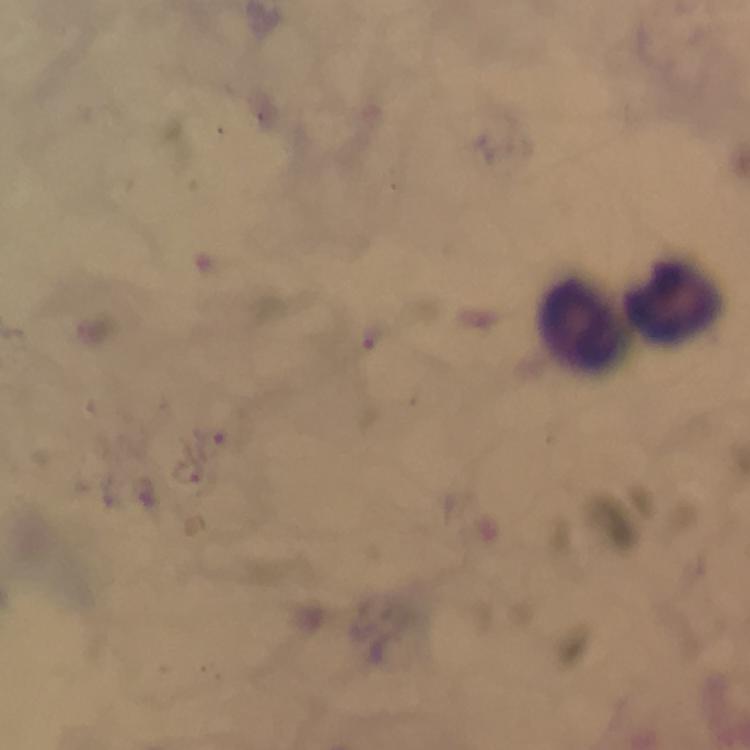
capture: smartphone camera through the microscope
immersion_oil: applied
context: from a diagnostic examination for malaria
magnification: 100x
plasmodium_parasite_locations: 'approximate object centers, in pixels from the top-left corner: (x=376, y=337)'
leukocyte_locations: 'approximate object centers, in pixels from the top-left corner: (x=673, y=303), (x=580, y=325)'
image_size: 750×750 pixels
preparation: thick blood smear
stain: Giemsa
cropped_from: a single field of view